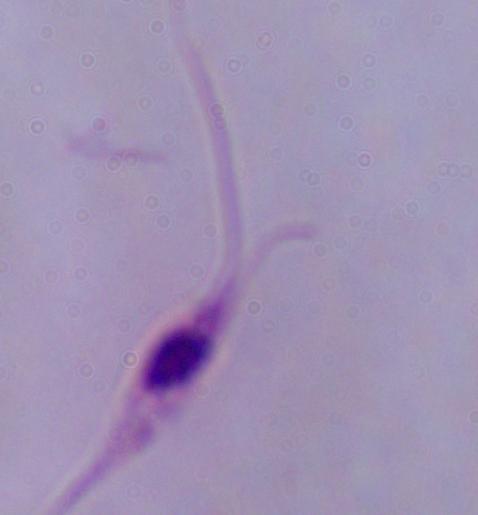

{
  "magnification": "1000x",
  "identification": "Leishmania",
  "modality": "micrograph"
}